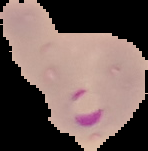 The area outside the segmented cell region is set to black. From a thin blood smear. Malaria status: parasitized. Image is 148×151 pixels.